Classify this cell by malaria status.
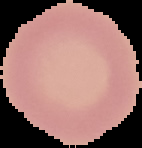

It is uninfected.

Summary:
  - Preparation: thin blood smear
  - Image type: segmented cell region on a black background
  - Image size: 142×148 pixels